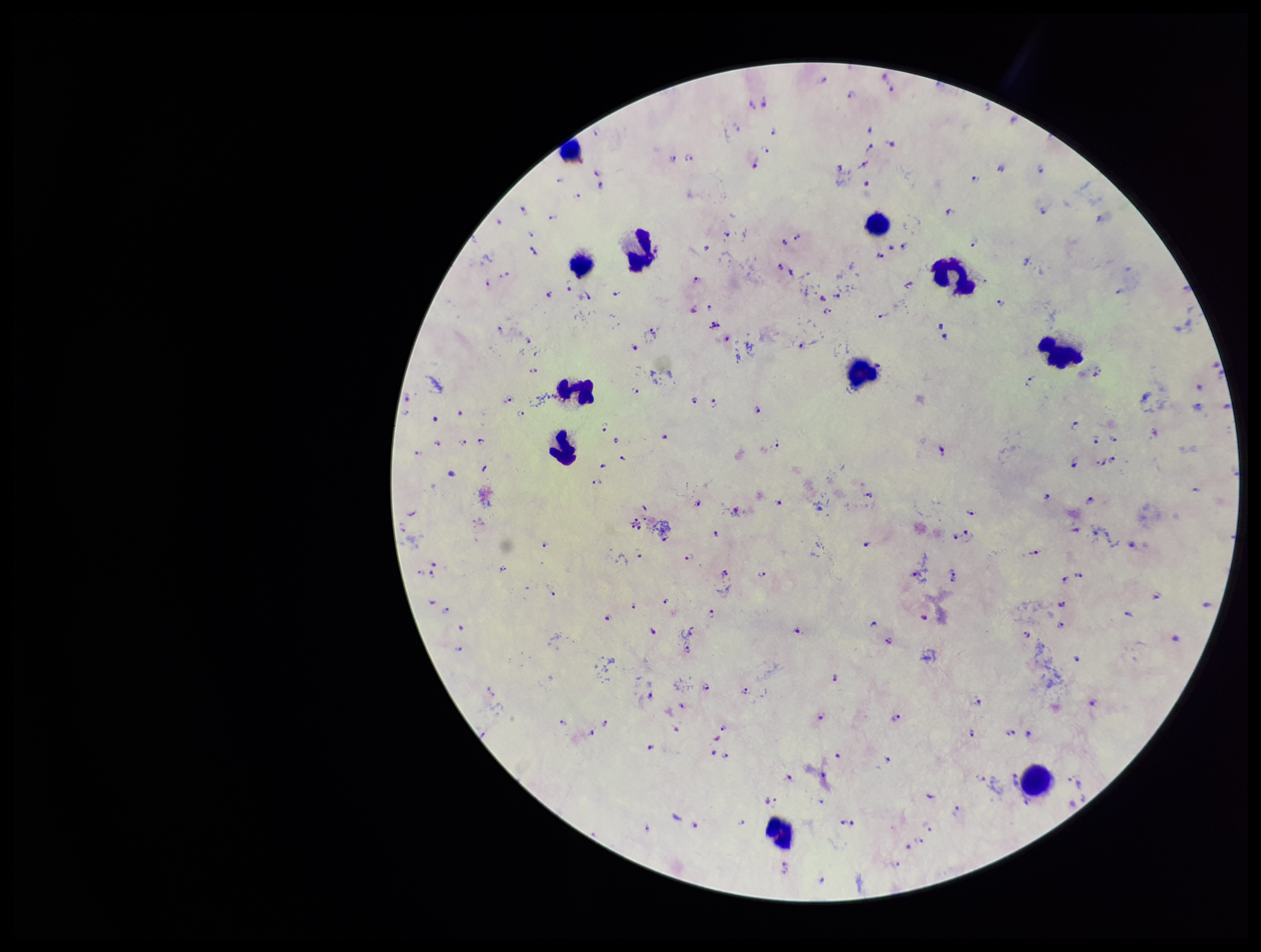 Giemsa stain. Preparation: thick blood smear. Leukocyte count: 11. Photographed through the microscope eyepiece with a smartphone camera. Image is 1261×952 pixels. Patient malaria status: infected. Parasite count: 167. Species reported for this patient: Plasmodium falciparum. Single field of view. Plasmodium parasites: identified.